Name the parasite shown.
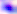

Toxoplasma gondii.

magnification = 400x
modality = photomicrograph